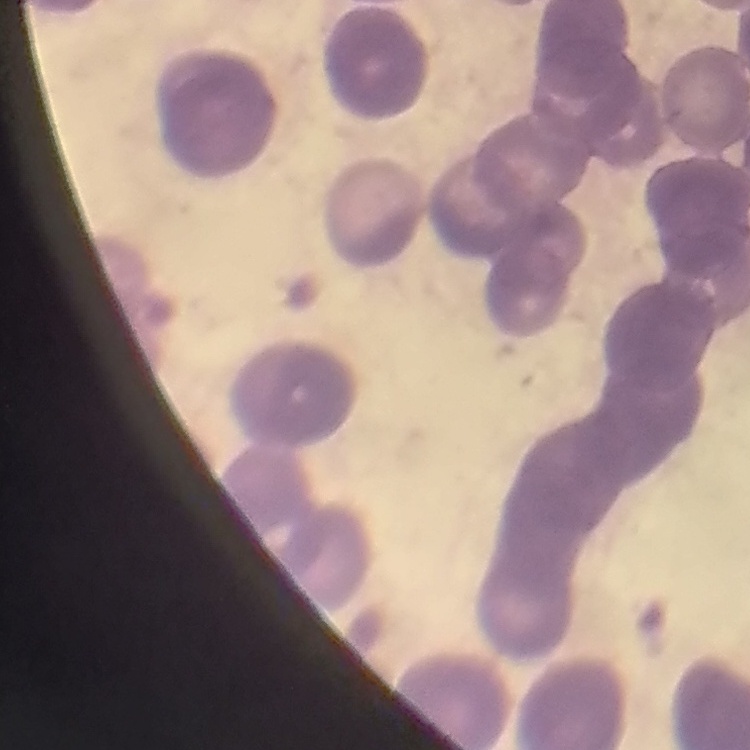

red blood cell morphology = rouleaux formation
stain = Field's or Giemsa
preparation = thin blood smear
image type = one tile cut from a larger photomicrograph